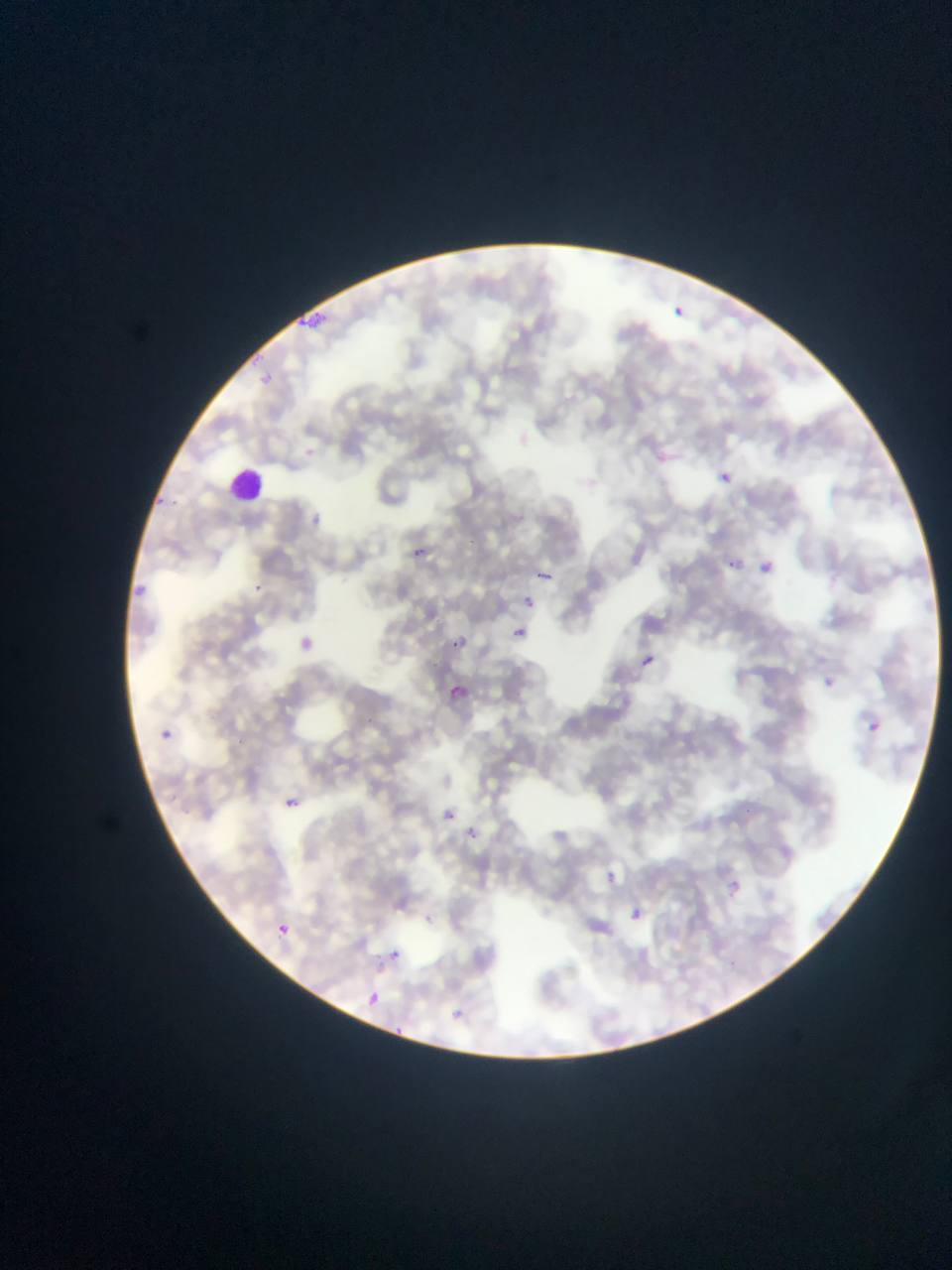

Approximate bounding boxes as left top right bottom in pixels.
Summary:
  - Plasmodium parasite locations: 673 306 687 318; 717 470 731 484; 412 547 429 557; 729 559 743 572; 756 561 771 574; 534 569 554 581; 524 595 538 611; 514 626 526 637; 454 636 471 652; 642 657 653 665; 448 685 467 700; 280 798 310 805; 440 810 457 824; 607 873 620 886; 728 879 739 895; 630 909 641 922; 277 922 288 938; 392 948 407 964; 365 989 380 1006; 392 1023 411 1033
  - Leukocyte locations: 228 463 271 509
  - Country: Ghana
  - Field of view: single
  - Preparation: thin blood film
  - Capture: mobile-phone photograph through a microscope
  - Image size: 952×1270 pixels